Assess this cell for malaria.
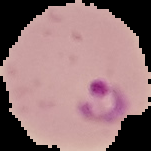
Parasitized.

preparation = thin blood smear
image size = 151×151 pixels
image type = segmented cell region with the area outside set to black